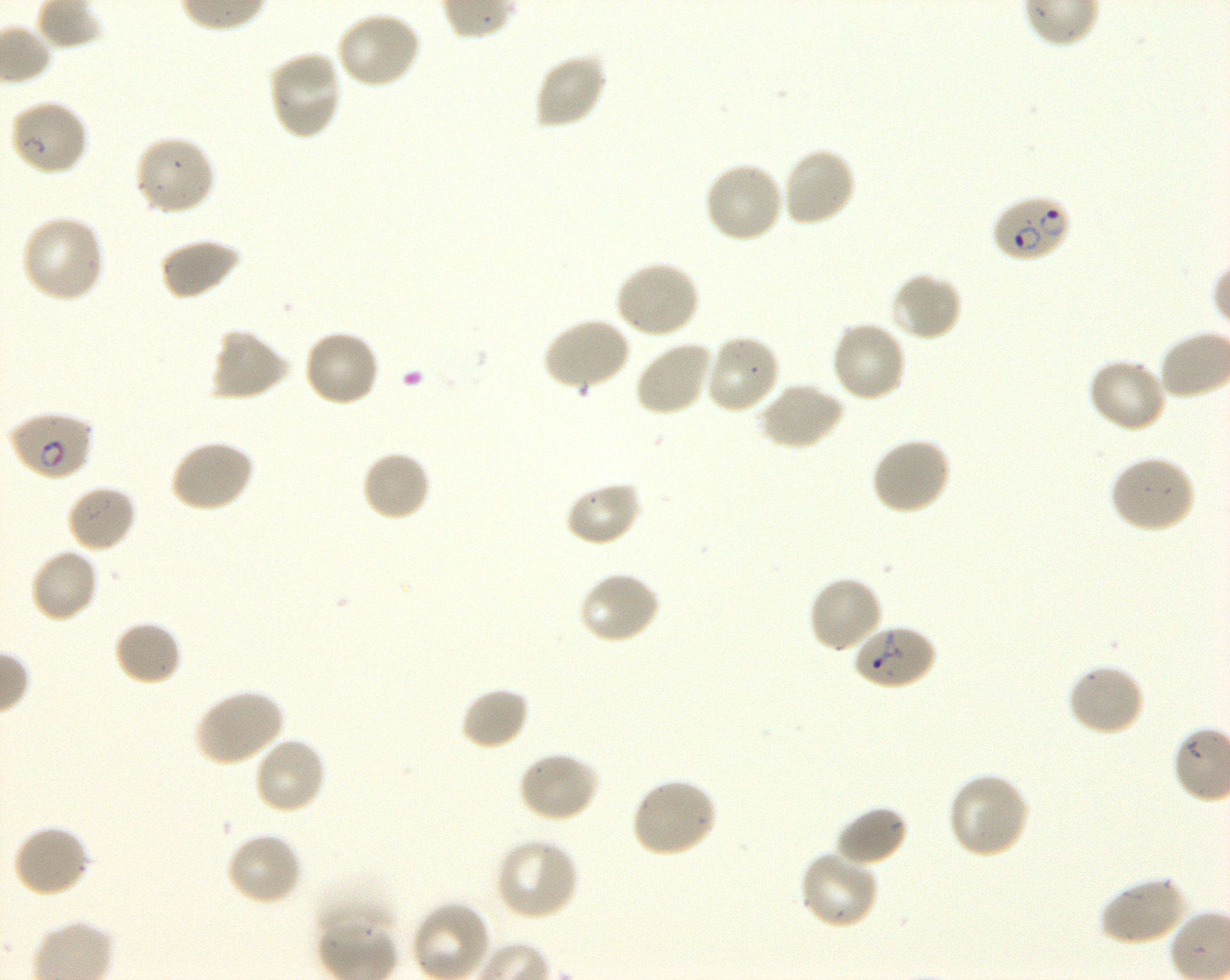 Approximate bounding boxes as {x1, y1, x2, y2} in pixels. Not every red blood cell is marked. A life-cycle stage — or a range of stages, where the recorded stages span more than one — follows each staged infected red blood cell. Locations of uninfected red blood cells: {334, 11, 421, 89}, {267, 51, 344, 142}, {533, 51, 608, 130}, {9, 99, 90, 178}, {134, 134, 217, 217}, {780, 145, 857, 228}, {703, 160, 783, 243}, {21, 215, 105, 304}, {159, 237, 241, 301}, {613, 258, 700, 339}, {889, 271, 962, 342}, {542, 317, 632, 393}, {830, 319, 908, 403}, {208, 326, 291, 402}, {303, 329, 380, 408}, {704, 333, 781, 416}, {634, 339, 713, 417}, {1087, 357, 1167, 434}, {757, 381, 844, 452}, {870, 435, 952, 515}, {168, 438, 255, 513}, {360, 449, 432, 522}, {1108, 455, 1197, 534}, {563, 480, 642, 547}, {66, 483, 138, 553}, {29, 546, 100, 624}, {577, 571, 662, 646}, {807, 574, 885, 654}, {115, 620, 183, 687}, {1066, 663, 1145, 737}, {459, 684, 531, 750}, {193, 688, 285, 766}, {253, 735, 327, 816}, {518, 750, 601, 824}, {946, 772, 1031, 860}, {630, 777, 717, 859}, {834, 804, 909, 868}, {12, 824, 92, 899}, {226, 831, 303, 905}, {495, 837, 580, 921}, {798, 850, 880, 930}, {315, 871, 396, 943}, {1099, 874, 1190, 946}, {412, 901, 491, 980}. Locations of infected red blood cells: {991, 194, 1071, 264} ring; {8, 410, 93, 481} early ring to early trophozoite. Locations of red blood cells of indeterminate infection status: {850, 623, 936, 691}. Thin blood film. 100x objective under oil immersion, numerical aperture 1.30. Image is 1230×980 pixels. Donor blood group O+. One field from this slide. Giemsa stain. P. falciparum strain 3D7 maintained in shaking in-vitro culture.